Report the malaria status of this cell.
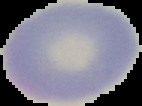

It is uninfected.

Image is 142×106 pixels. From a thin blood film. The area outside the segmented cell region is set to black.